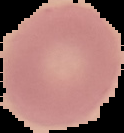

image size = 124×133 pixels
malaria status = uninfected
preparation = thin blood film
image type = segmented cell region on a black background